Outline each blood parasite and name the species.
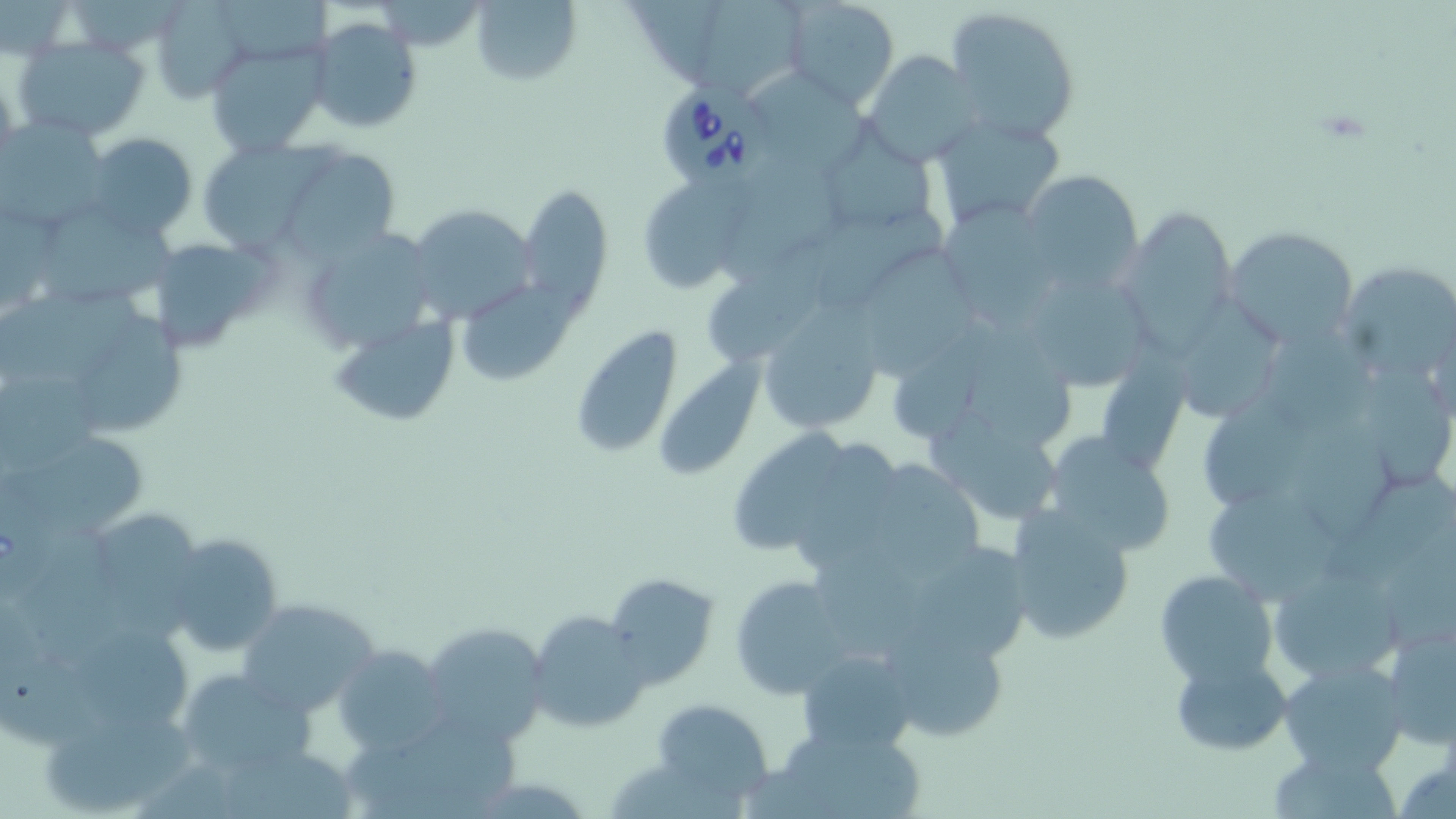
Approximate bounding boxes as [x1, y1, x2, y2] in pixels.
Babesia divergens-infected red blood cells: [655, 86, 768, 185], [0, 484, 57, 600].
No Plasmodium falciparum, Plasmodium ovale, Plasmodium malariae, Plasmodium vivax, or Trypanosoma brucei observed.

slide-level diagnosis = Babesia divergens
stain = May-Grünwald-Giemsa
preparation = thin blood smear
field of view = single
modality = light microscopy
image size = 1456×819 pixels
magnification = 1000x
uninfected red blood cell locations = approximate bounding boxes as [x1, y1, x2, y2] in pixels: [217, 0, 332, 61], [470, 0, 581, 85], [627, 0, 729, 84], [705, 0, 813, 82], [784, 0, 900, 109], [152, 1, 250, 101], [943, 5, 1081, 144], [304, 16, 424, 135], [13, 36, 152, 144], [204, 40, 330, 159], [861, 51, 982, 166], [754, 74, 879, 176], [929, 113, 1065, 232], [2, 117, 110, 229], [815, 129, 939, 238], [84, 133, 197, 240], [195, 139, 327, 253], [269, 144, 404, 261], [1020, 169, 1144, 295], [719, 174, 844, 289], [637, 175, 746, 294], [514, 184, 611, 306], [942, 196, 1048, 332], [40, 201, 179, 302], [404, 203, 537, 326], [1117, 206, 1242, 355], [817, 212, 946, 315], [306, 225, 427, 350], [1225, 226, 1364, 348], [154, 234, 274, 352], [707, 236, 855, 362], [865, 243, 979, 378], [1336, 260, 1456, 390], [461, 278, 586, 382], [1043, 285, 1139, 392], [0, 287, 146, 384], [1182, 304, 1280, 421], [754, 306, 891, 438], [90, 314, 183, 433], [329, 315, 462, 431], [569, 327, 686, 458], [898, 329, 994, 441], [1272, 330, 1376, 445], [976, 338, 1072, 455], [662, 347, 770, 486], [1097, 359, 1189, 475], [1363, 367, 1450, 488], [2, 375, 106, 470], [1205, 395, 1310, 508], [933, 414, 1056, 520], [733, 415, 854, 550], [1299, 427, 1395, 538], [1052, 429, 1179, 553], [6, 436, 149, 526], [801, 438, 902, 568], [874, 461, 984, 583], [1333, 472, 1454, 582], [1212, 497, 1338, 601], [1004, 503, 1137, 643], [104, 518, 200, 596], [25, 527, 142, 665], [166, 533, 285, 657], [816, 543, 930, 663], [914, 547, 1029, 659], [1264, 560, 1415, 684], [1380, 565, 1456, 650], [1155, 568, 1280, 687], [604, 573, 719, 688], [731, 576, 847, 696], [232, 597, 384, 716], [526, 609, 652, 734], [1379, 612, 1456, 750], [421, 619, 551, 745], [882, 622, 1012, 744], [81, 633, 191, 732], [334, 645, 451, 754], [797, 649, 918, 758], [0, 653, 95, 749], [1169, 653, 1293, 756], [1275, 658, 1409, 776], [171, 667, 317, 782], [654, 699, 773, 805], [384, 708, 522, 805], [41, 711, 197, 815], [778, 722, 927, 819], [227, 749, 353, 819], [1271, 752, 1407, 819]